Identify the parasite.
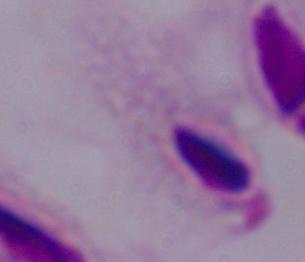
This is a trichomonad.

{
  "magnification": "1000x",
  "modality": "photomicrograph"
}